Locate every blood parasite and identify its species.
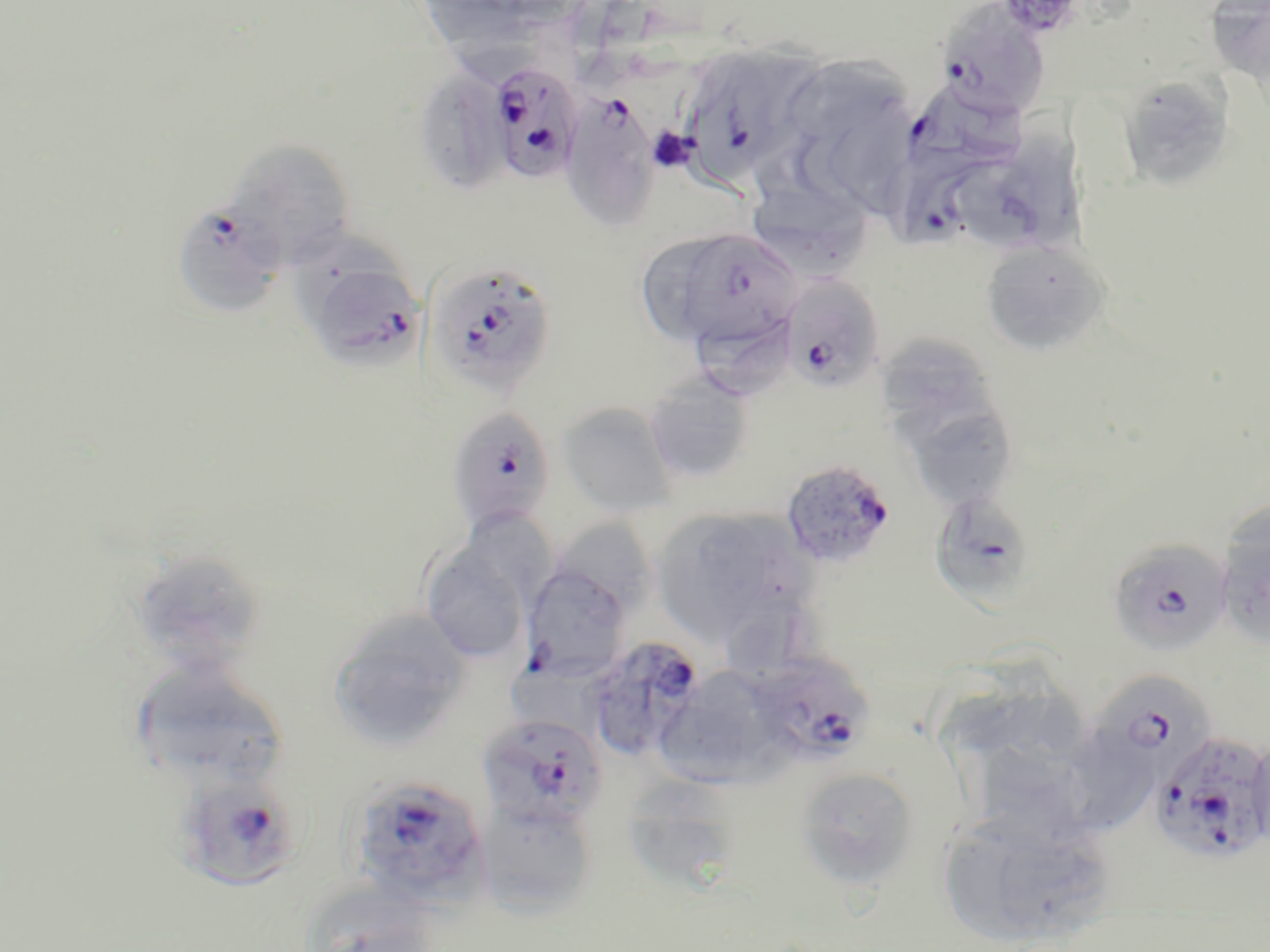

Approximate bounding boxes as (x1, y1, x2, y2) in pixels.
Plasmodium falciparum-infected red blood cells: (936, 3, 1051, 118), (678, 45, 823, 182), (487, 61, 585, 185), (905, 85, 1029, 178), (558, 90, 662, 231), (882, 151, 1000, 254), (171, 200, 286, 319), (692, 227, 804, 353), (296, 253, 426, 372), (440, 267, 554, 388), (779, 274, 886, 393), (444, 405, 557, 533), (780, 458, 896, 570), (929, 492, 1038, 606), (1106, 538, 1233, 657), (520, 559, 634, 682), (582, 637, 706, 762), (750, 654, 874, 766), (1094, 677, 1222, 794), (477, 712, 608, 831), (1150, 729, 1270, 865), (174, 772, 303, 891), (346, 774, 489, 906).
No Plasmodium ovale, Plasmodium malariae, Plasmodium vivax, Babesia divergens, or Trypanosoma brucei observed.

slide-level diagnosis = Plasmodium falciparum
platelet locations = approximate bounding boxes as (x1, y1, x2, y2) in pixels: (648, 128, 696, 171)
stain = May-Grünwald-Giemsa
uninfected red blood cell locations = approximate bounding boxes as (x1, y1, x2, y2) in pixels: (424, 0, 529, 84), (1205, 1, 1270, 91), (793, 49, 910, 139), (415, 65, 513, 196), (1116, 75, 1235, 192), (829, 98, 918, 214), (968, 132, 1098, 249), (224, 138, 357, 268), (746, 179, 873, 281), (639, 235, 732, 339), (980, 240, 1111, 356), (697, 314, 792, 403), (882, 333, 1007, 438), (643, 373, 755, 484), (902, 399, 1019, 510), (558, 402, 678, 516), (651, 505, 812, 648), (1214, 509, 1270, 650), (557, 525, 660, 608), (420, 537, 534, 666), (128, 547, 267, 676), (327, 610, 472, 751), (128, 661, 291, 792), (662, 665, 787, 791), (938, 669, 1067, 755), (1068, 728, 1153, 827), (965, 730, 1086, 845), (795, 766, 920, 889), (630, 772, 730, 887), (475, 796, 599, 917), (938, 808, 1116, 948), (297, 877, 440, 952)
image size = 1270×952 pixels
magnification = 1000x
preparation = thin blood smear
field of view = single
modality = optical microscopy